Report the malaria status of this cell.
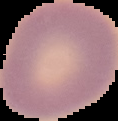
Uninfected.

From a thin blood film. Image is 118×121 pixels. Cell region segmented out of the field of view; the surrounding area is masked to black.